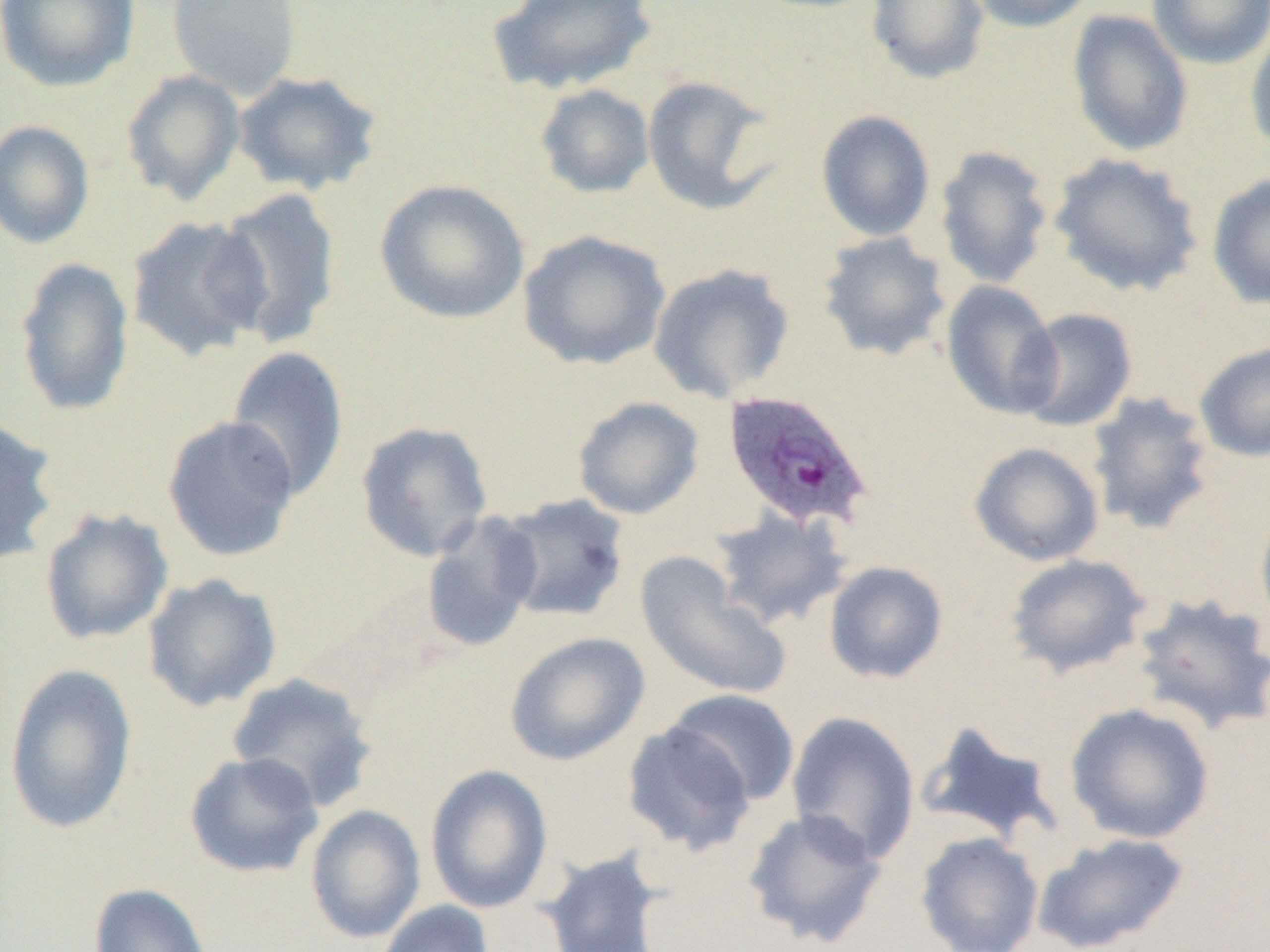
Approximate bounding boxes as (x1,y1)-(x2,y2) corner pairs in pixels. Plasmodium ovale-infected red blood cell locations: (722,390)-(873,532). Uninfected red blood cell locations: (166,0)-(302,101), (489,0)-(657,96), (865,0)-(991,85), (962,0)-(1098,33), (1146,0)-(1270,69), (0,1)-(139,91), (1066,10)-(1194,157), (1245,20)-(1270,156), (120,69)-(246,206), (232,70)-(384,196), (641,75)-(781,217), (535,84)-(655,199), (816,109)-(936,242), (0,120)-(95,249), (934,145)-(1054,289), (1048,152)-(1204,298), (1206,172)-(1270,310), (374,178)-(531,325), (214,188)-(342,348), (125,214)-(272,363), (517,230)-(671,370), (817,231)-(952,362), (14,256)-(135,417), (648,263)-(795,403), (940,280)-(1062,420), (1015,307)-(1138,432), (1193,341)-(1270,463), (226,345)-(350,502), (1086,390)-(1217,534), (573,396)-(704,519), (0,414)-(61,567), (162,415)-(300,562), (355,421)-(494,563), (969,442)-(1104,566), (496,493)-(631,623), (1254,495)-(1270,640), (711,507)-(853,631), (39,508)-(174,645), (420,511)-(543,653), (635,552)-(793,702), (1004,554)-(1153,679), (823,561)-(949,684), (142,573)-(282,712), (1130,592)-(1270,737), (504,632)-(650,766), (4,663)-(138,836), (225,671)-(380,813), (664,688)-(801,806), (1065,702)-(1215,845), (785,710)-(921,865), (915,719)-(1067,847), (622,721)-(757,856), (185,751)-(324,879), (426,764)-(554,914), (305,804)-(426,944), (742,807)-(888,949), (915,831)-(1044,952), (1033,832)-(1189,952), (536,846)-(671,952), (88,883)-(213,952), (374,900)-(495,951). Slide-level diagnosis: Plasmodium ovale. Thin blood smear. Optical microscopy. Captured at 1000x magnification. Single field of view. Image is 1270×952 pixels.